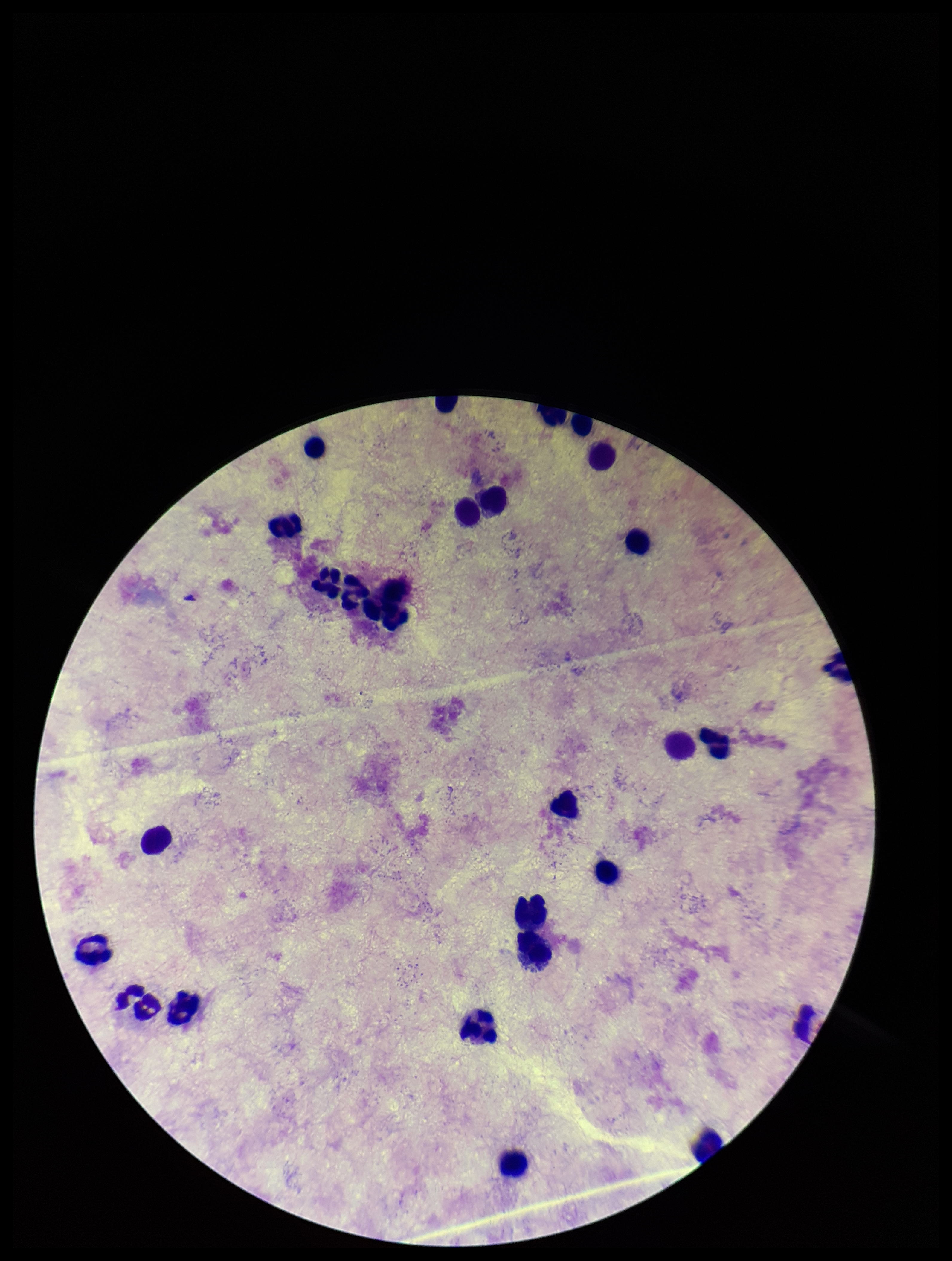
capture = smartphone photograph through the microscope eyepiece
parasite count = 0
leukocyte count = 26
stain = Giemsa
patient malaria status = negative
field of view = single
preparation = thick smear
image size = 952×1261 pixels
Plasmodium parasites = none seen